Name the parasite shown.
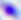
This is Toxoplasma gondii.

Summary:
  - Modality: photomicrograph
  - Magnification: 400x